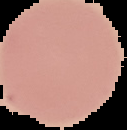
Image is 127×130 pixels. The area outside the segmented cell region is set to black. From a thin blood film. Result: no malaria parasites seen.